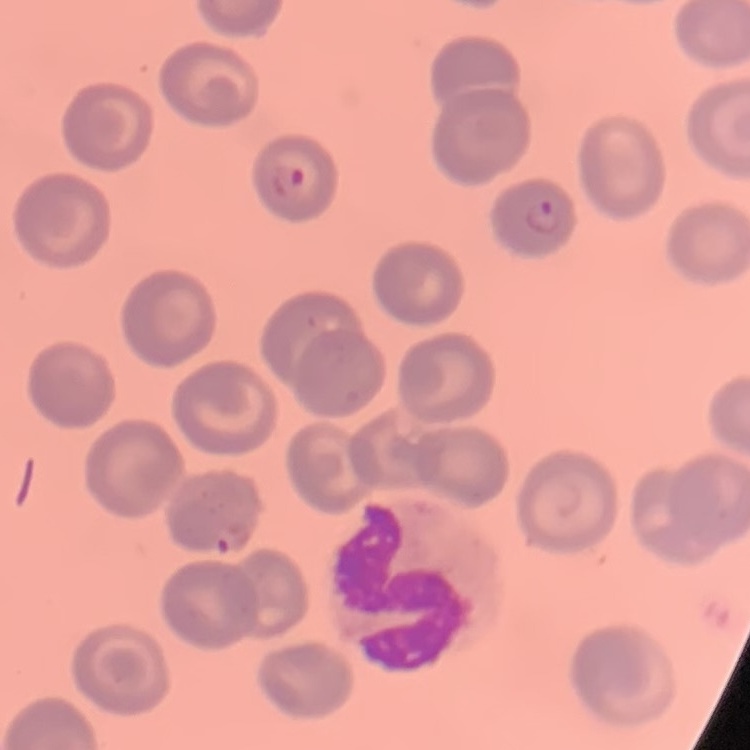
red blood cell morphology = no rouleaux formation
image type = square crop of a larger photomicrograph
stain = Field's or Giemsa
preparation = thin peripheral smear